Assess for Plasmodium parasites.
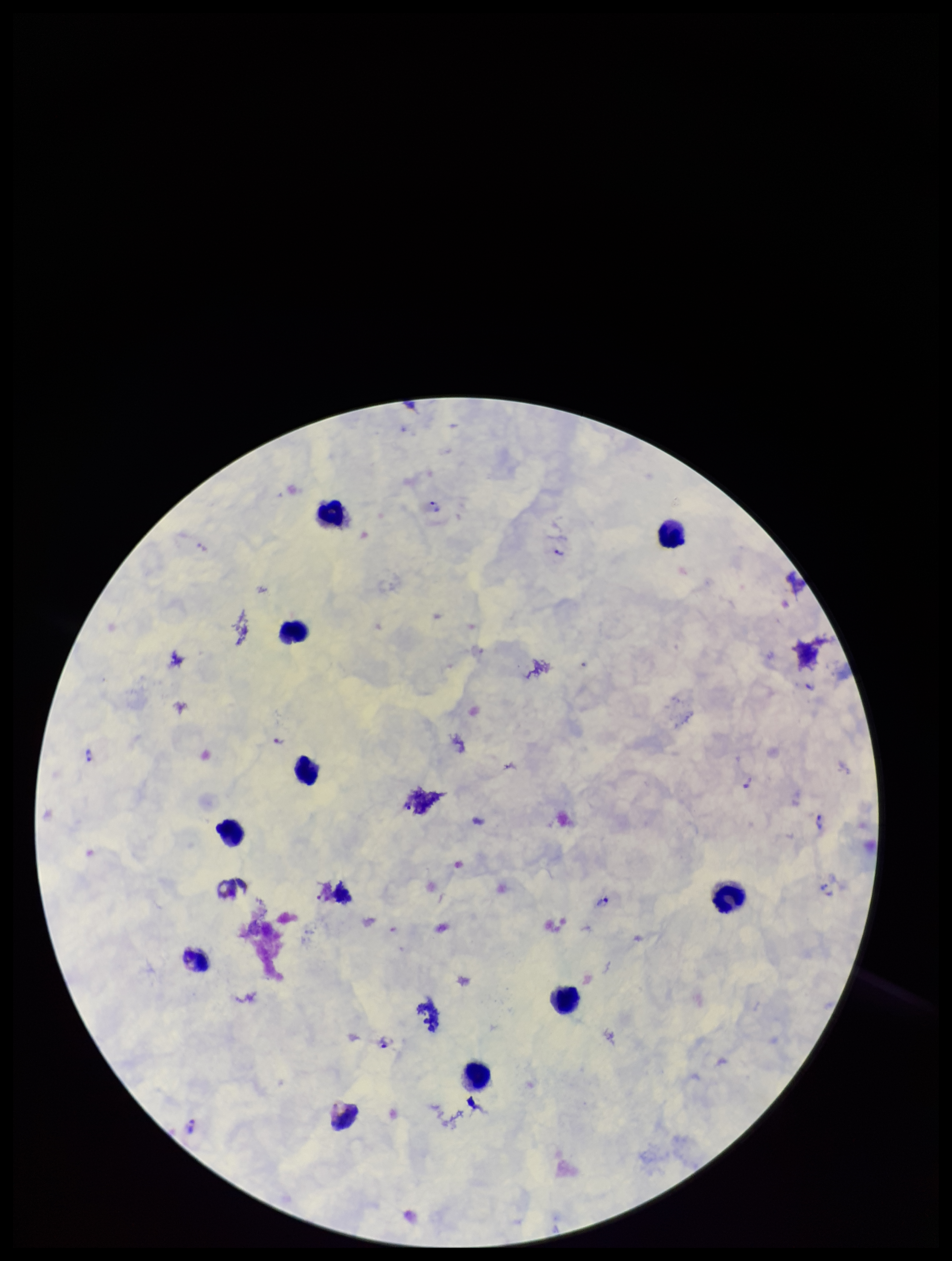
Identified.

Photographed through the microscope eyepiece with a smartphone camera. Image is 952×1261 pixels. Parasite count: 11. Single field of view. Preparation: thick blood smear. Leukocyte count: 10. Species reported for this patient: Plasmodium vivax. Giemsa stain. Patient malaria status: positive.